Assess for Plasmodium parasites.
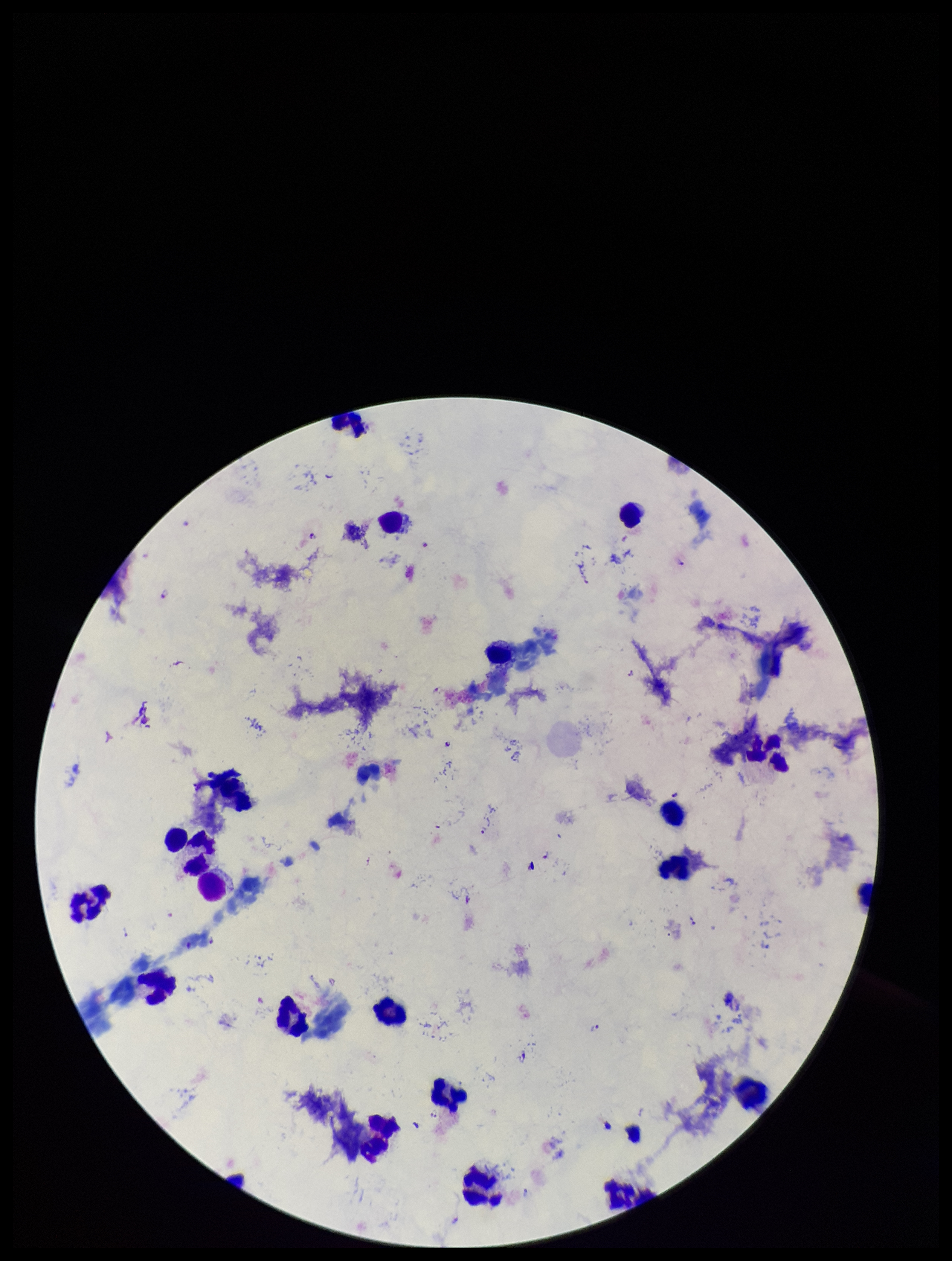
Seen.

Single field of view. Preparation: thick smear. Parasite count: 10. Patient malaria status: infected. Giemsa stain. Image is 952×1261 pixels. Leukocyte count: 20. Photographed through the microscope eyepiece with a smartphone camera. Species reported for this patient: Plasmodium falciparum.